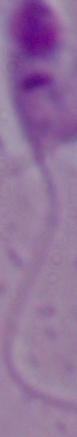

identification = Leishmania
magnification = 1000x
modality = micrograph